Point out Plasmodium parasites and leukocytes.
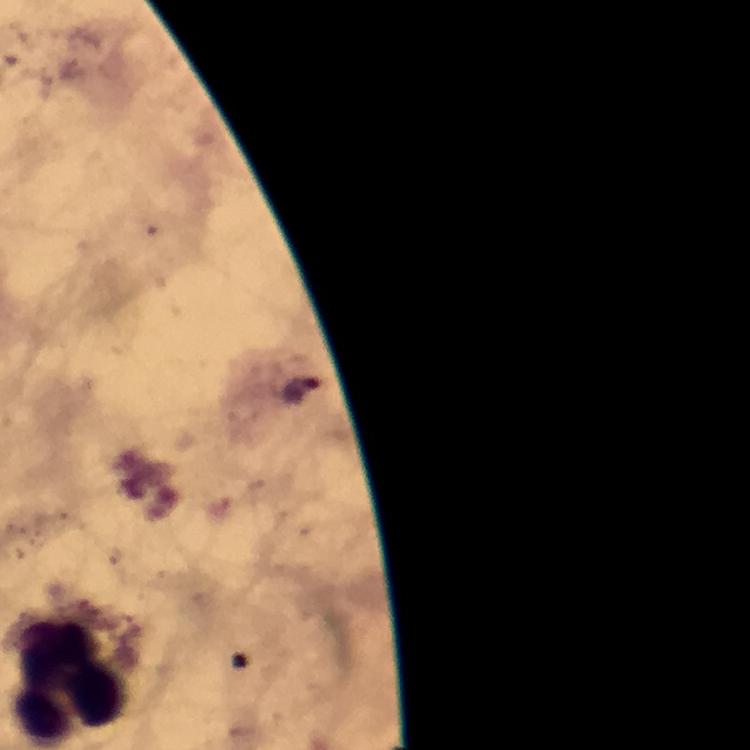

No Plasmodium parasites detected.
Approximate centers as (x, y) in pixels.
Leukocytes: (71, 677).

Immersion oil was used. 100x magnification. Photographed with a smartphone mounted on the microscope. From a diagnostic examination for malaria. Image is 750×750 pixels. Giemsa stain. Thick blood film. A crop from one field of view.